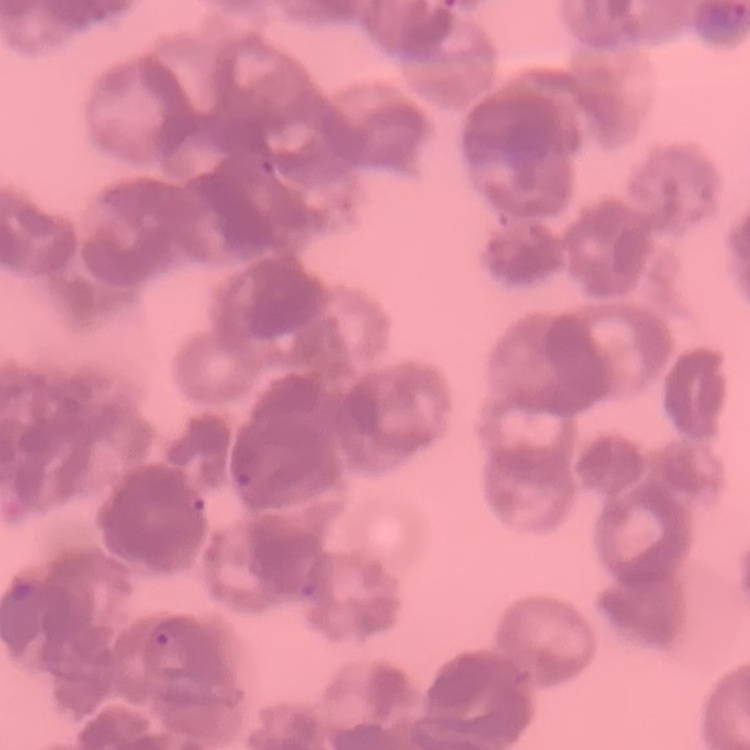

The red blood cells exhibit rouleaux formation. Stained with either Field's or Giemsa. Square crop of a larger photomicrograph. Thin blood smear.